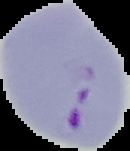 Malaria status: parasitized. From a thin blood film. Image is 130×151 pixels. Segmented cell region on a black background.